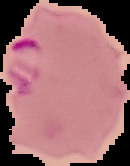
Malaria status: parasitized. The area outside the segmented cell region is set to black. Image is 130×166 pixels. From a thin blood smear.